Name the cell type shown.
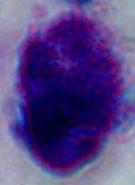
A leukocyte.

{
  "modality": "photomicrograph",
  "magnification": "1000x"
}